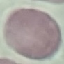
Result: no malaria parasites seen. Thin blood smear. Acquired by smartphone through the microscope eyepiece. Cell patch, automatically extracted from a larger field of view and resized to 64 × 64 pixels. Giemsa-stained preparation.